Point out every malaria parasite.
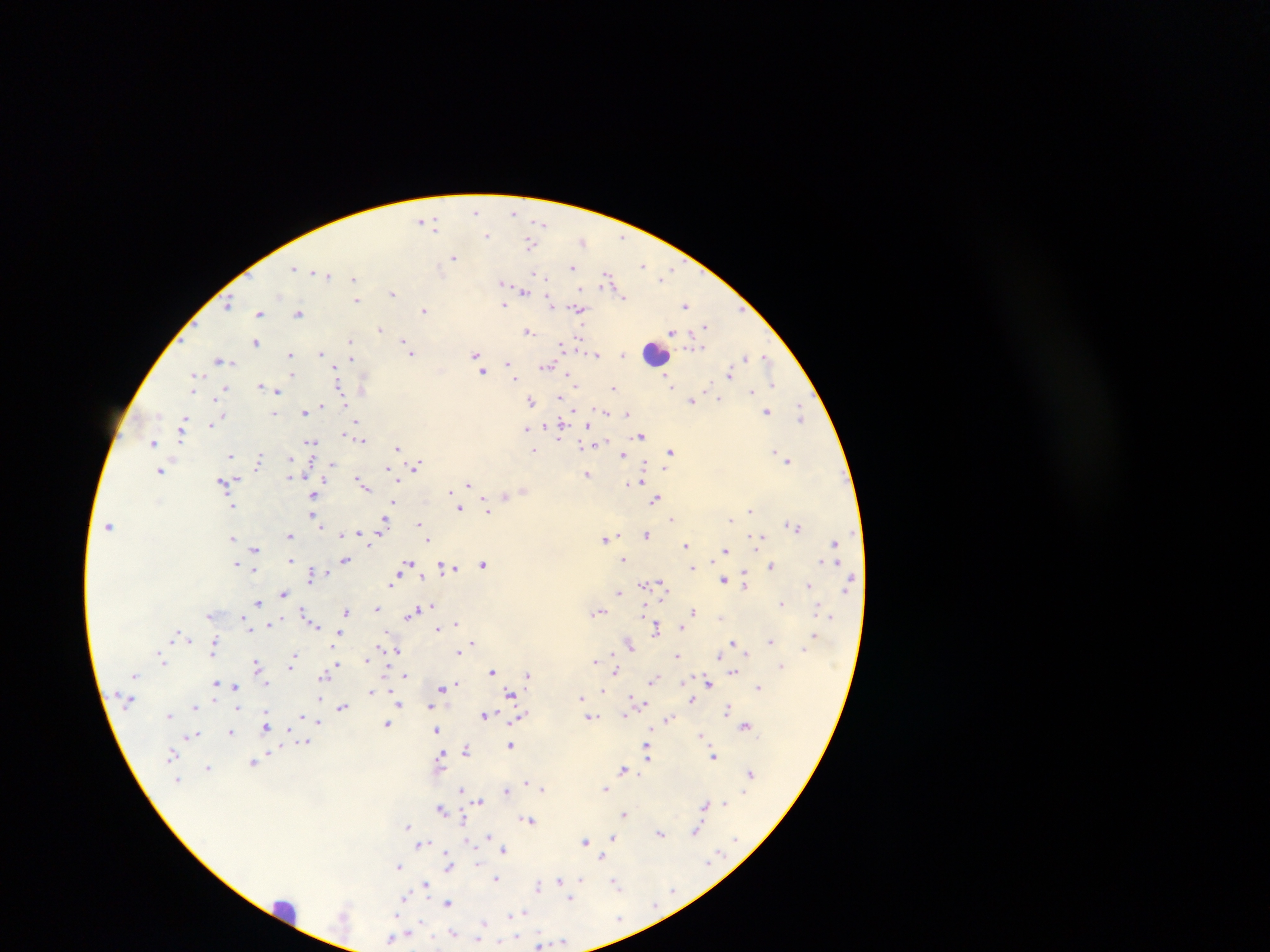
Approximate centers as [x, y] in pixels.
Malaria parasites: [476, 211], [514, 212], [422, 220], [427, 220], [541, 223], [435, 224], [486, 235], [622, 237], [583, 241], [530, 244], [453, 256], [643, 264], [573, 266], [294, 268], [672, 270], [327, 274], [535, 274], [541, 274], [607, 277], [663, 277], [354, 279], [503, 283], [503, 288], [523, 290], [392, 293], [622, 296], [356, 300], [550, 303], [229, 304], [685, 305], [503, 306], [579, 308], [424, 310], [259, 313], [298, 313], [706, 327], [381, 329], [527, 330], [671, 332], [578, 339], [256, 342], [350, 342], [561, 344], [321, 353], [411, 353], [476, 354], [597, 354], [623, 354], [290, 355], [746, 357], [766, 357], [220, 360], [351, 360], [507, 363], [546, 367], [509, 368], [335, 371], [483, 371], [729, 373], [292, 375], [194, 377], [569, 378], [515, 379], [773, 383], [574, 384], [670, 385], [260, 386], [339, 387], [613, 388], [193, 389], [224, 390], [276, 390], [752, 391], [342, 394], [217, 398], [559, 398], [719, 399], [692, 400], [531, 401], [322, 406], [600, 409], [574, 410], [767, 411], [304, 412], [608, 412], [800, 413], [274, 414], [627, 414], [184, 418], [220, 418], [356, 422], [212, 424], [183, 427], [560, 427], [526, 428], [346, 433], [641, 436], [558, 439], [362, 440], [152, 442], [311, 442], [585, 445], [397, 447], [534, 450], [670, 452], [776, 452], [231, 455], [623, 456], [289, 459], [259, 460], [788, 460], [332, 465], [417, 466], [644, 467], [389, 469], [160, 472], [586, 474], [290, 475], [640, 479], [224, 482], [360, 482], [637, 483], [469, 484], [363, 485], [314, 495], [505, 496], [656, 499], [393, 503], [233, 506], [459, 508], [486, 509], [751, 511], [313, 517], [672, 517], [731, 519], [316, 520], [384, 522], [789, 524], [420, 525], [109, 526], [796, 526], [361, 533], [343, 534], [646, 535], [289, 536], [425, 536], [232, 537], [761, 537], [428, 539], [604, 539], [834, 543], [685, 546], [254, 550], [726, 550], [623, 559], [291, 560], [346, 560], [824, 561], [236, 564], [408, 564], [483, 564], [771, 566], [691, 567], [451, 569], [312, 573], [723, 579], [745, 582], [390, 583], [663, 584], [809, 585], [643, 586], [618, 592], [284, 593], [258, 603], [782, 604], [376, 608], [644, 608], [600, 611], [693, 611], [346, 612], [414, 613], [306, 614], [209, 616], [310, 621], [245, 622], [272, 622], [314, 624], [457, 624], [656, 628], [682, 628], [438, 629], [176, 634], [338, 634], [814, 634], [190, 640], [771, 641], [732, 642], [473, 643], [630, 645], [803, 647], [215, 648], [397, 650], [458, 653], [747, 653], [295, 655], [719, 655], [677, 656], [368, 659], [162, 661], [595, 661], [336, 663], [256, 665], [780, 665], [291, 666], [492, 671], [615, 672], [733, 672], [324, 675], [405, 675], [527, 675], [653, 679], [215, 682], [708, 682], [221, 685], [456, 686], [235, 687], [758, 687], [443, 688], [371, 692], [602, 692], [511, 694], [582, 697], [632, 697], [692, 700], [638, 703], [398, 704], [196, 707], [342, 707], [430, 707], [728, 709], [169, 715], [485, 715], [625, 716], [521, 717], [592, 717], [668, 719], [318, 722], [387, 724], [266, 725], [745, 725], [436, 730], [231, 732], [193, 736], [701, 736], [306, 742], [511, 745], [467, 748], [172, 754], [649, 754], [713, 756], [440, 759], [253, 763], [208, 768], [623, 770], [749, 773], [177, 781], [527, 782], [461, 789], [543, 789], [605, 789], [506, 791], [480, 801], [705, 803], [723, 804], [442, 809], [625, 813], [530, 820], [407, 827], [696, 831], [661, 833], [489, 836], [613, 837], [585, 841], [468, 842], [422, 844], [504, 850], [602, 857], [477, 863], [449, 865], [398, 866], [497, 878], [581, 879], [559, 881], [425, 884], [616, 884], [538, 886], [404, 897], [571, 899], [449, 903], [522, 913], [512, 914], [484, 924], [453, 932], [393, 939], [562, 942], [540, 943].

preparation = thick blood film
leukocyte locations = approximate centers as [x, y] in pixels: [656, 354], [285, 910]
field of view = single
country = Ghana
capture = mobile-phone photograph through a microscope
image size = 1270×952 pixels